Locate every malaria parasite.
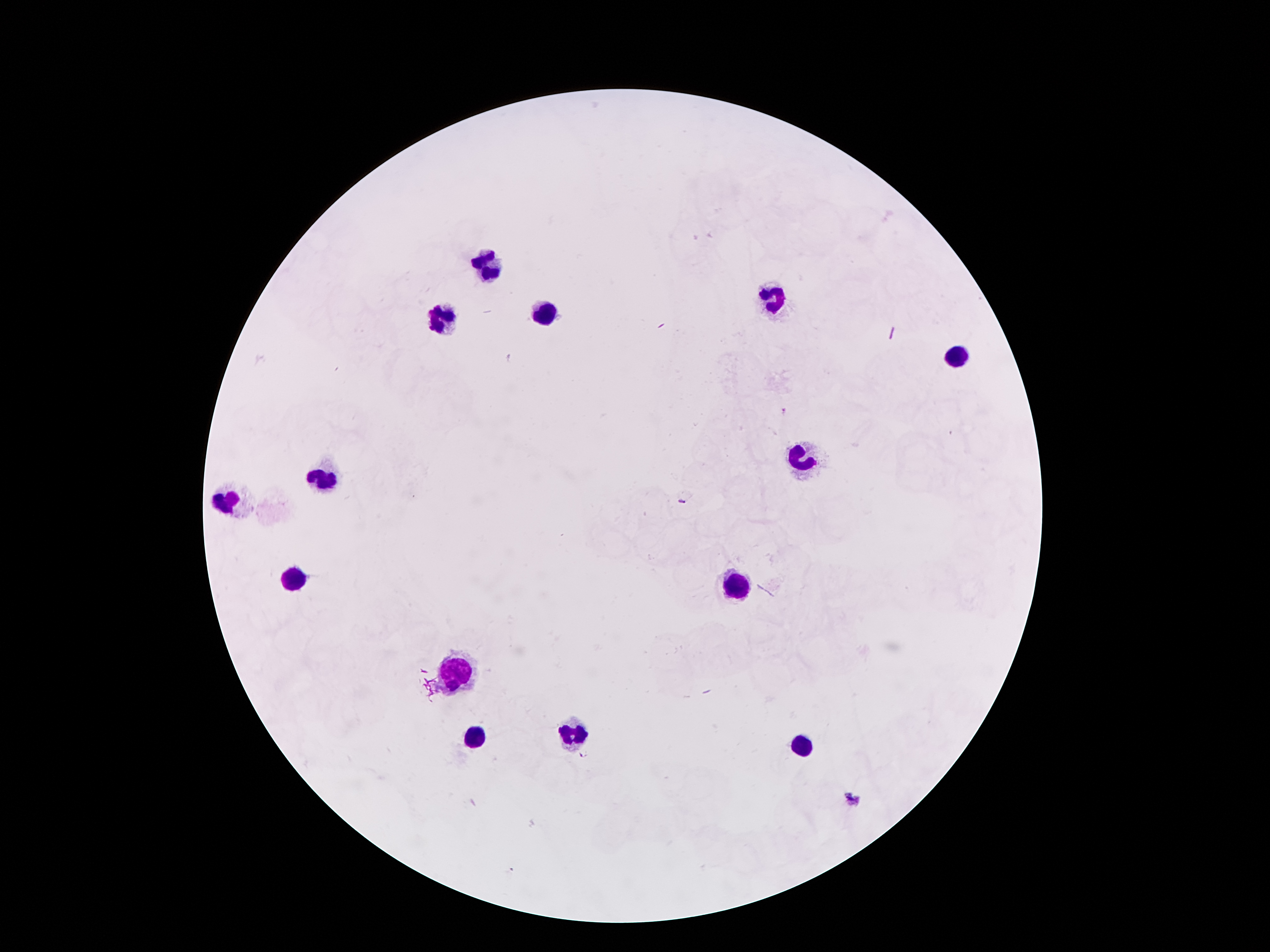
Approximate centers as (x, y) in pixels.
Malaria parasites: (783, 411), (584, 754), (852, 799).

Leukocyte locations: (490, 267), (774, 301), (545, 312), (443, 321), (960, 355), (801, 457), (318, 478), (225, 500), (293, 576), (733, 587), (456, 673), (575, 732), (475, 735), (804, 748). Giemsa stain. One field from this slide. Image is 1270×952 pixels. Thick peripheral-blood smear. Smartphone photograph taken through the microscope eyepiece. Patient malaria status: infected with Plasmodium falciparum. 100x magnification.